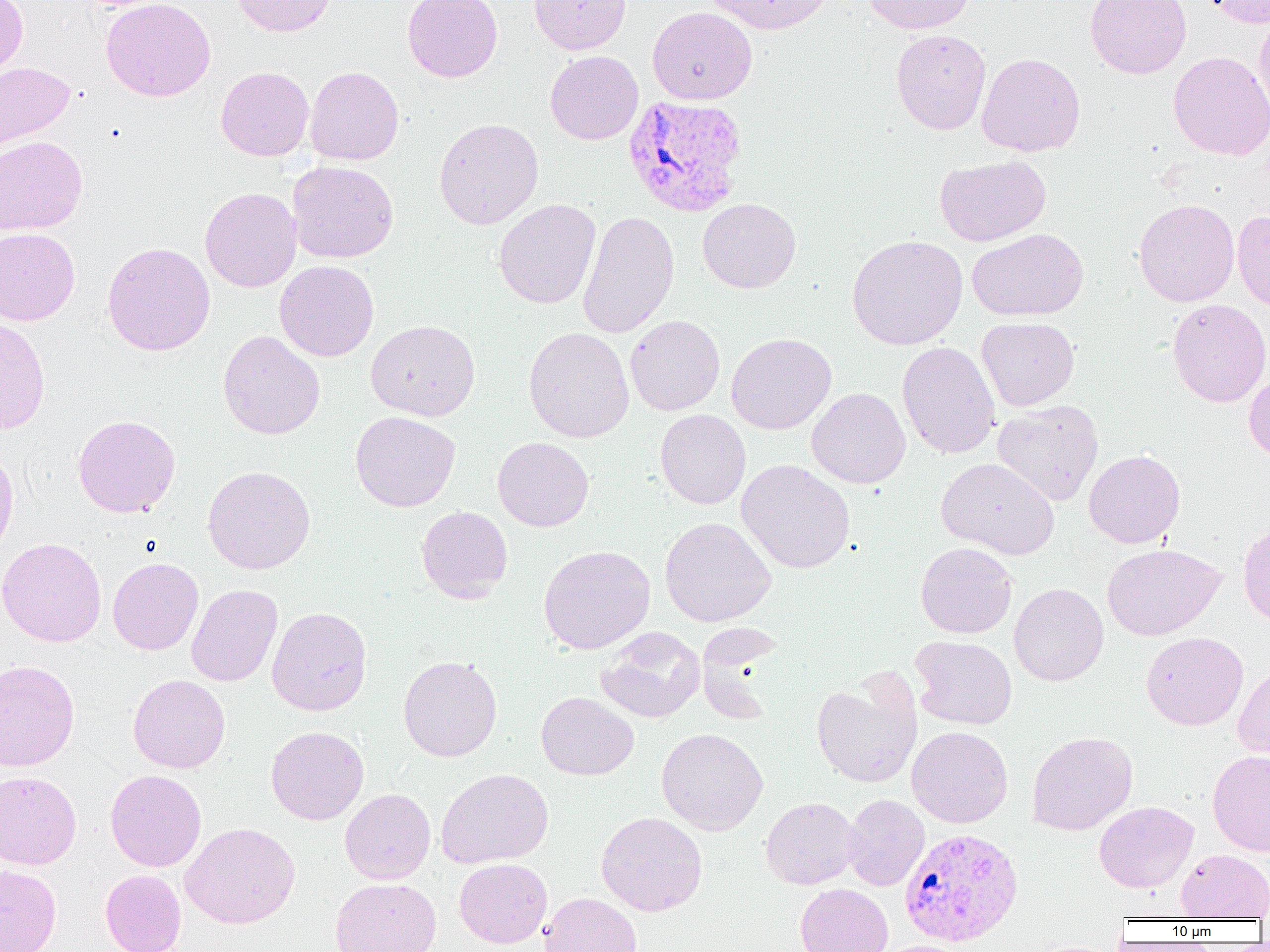
{
  "slide_level_diagnosis": "Plasmodium vivax",
  "magnification": "1000x",
  "preparation": "thin blood smear",
  "uninfected_red_blood_cell_locations": "approximate bounding boxes as (x1, y1, x2, y2) in pixels: (0, 0, 28, 80), (100, 0, 216, 102), (232, 0, 336, 37), (403, 0, 503, 82), (530, 0, 631, 54), (702, 0, 834, 34), (862, 0, 975, 34), (1085, 0, 1192, 79), (1205, 0, 1270, 28), (647, 7, 757, 105), (1253, 11, 1270, 123), (891, 29, 991, 134), (545, 51, 643, 144), (1168, 51, 1270, 161), (976, 52, 1085, 157), (0, 62, 75, 156), (216, 66, 314, 161), (305, 66, 404, 165), (434, 118, 544, 229), (0, 135, 87, 236), (934, 155, 1051, 247), (287, 160, 399, 264), (200, 187, 302, 292), (697, 198, 801, 293), (1134, 198, 1240, 307), (494, 199, 600, 309), (1232, 209, 1270, 312), (578, 210, 679, 339), (0, 228, 80, 326), (968, 228, 1088, 321), (847, 234, 968, 350), (102, 242, 215, 356), (275, 260, 378, 362), (1167, 298, 1270, 407), (625, 315, 725, 415), (0, 316, 50, 434), (977, 316, 1080, 411), (366, 319, 480, 421), (523, 327, 634, 442), (218, 330, 325, 439), (726, 333, 836, 434), (897, 341, 1000, 459), (1243, 368, 1270, 462), (806, 387, 911, 488), (992, 401, 1104, 506), (655, 409, 751, 509), (350, 411, 460, 511), (72, 414, 181, 518), (493, 437, 594, 531), (0, 445, 19, 560), (1084, 450, 1185, 548), (935, 457, 1060, 559), (736, 459, 856, 573), (202, 466, 315, 574), (416, 505, 513, 602), (659, 516, 776, 627), (1238, 521, 1270, 626), (0, 537, 107, 647), (915, 542, 1017, 638), (1102, 543, 1225, 641), (538, 544, 656, 654), (108, 557, 203, 655), (1009, 583, 1108, 686), (186, 584, 282, 687), (267, 606, 372, 716), (595, 627, 706, 723), (1141, 632, 1248, 730), (910, 635, 1017, 730), (398, 655, 502, 761), (0, 660, 80, 772), (1233, 664, 1270, 764), (811, 672, 922, 787), (128, 674, 230, 773), (536, 691, 638, 780), (265, 726, 369, 824), (907, 726, 1013, 827), (656, 727, 768, 836), (1026, 731, 1138, 836), (1208, 750, 1270, 856), (436, 768, 553, 868), (105, 769, 206, 871), (0, 771, 81, 870), (340, 788, 436, 884), (842, 794, 929, 891), (760, 796, 862, 889), (1093, 801, 1198, 892), (596, 811, 708, 916), (180, 822, 300, 928), (1176, 849, 1270, 920), (454, 858, 552, 948), (0, 864, 61, 952), (100, 869, 186, 952), (330, 878, 441, 952), (795, 883, 893, 952), (539, 892, 642, 952), (877, 940, 976, 952)",
  "modality": "light microscopy",
  "image_size": "1270×952 pixels",
  "field_of_view": "single",
  "plasmodium_vivax_infected_red_blood_cell_locations": "approximate bounding boxes as (x1, y1, x2, y2) in pixels: (623, 94, 748, 217), (899, 827, 1023, 946)"
}